Classify this cell by malaria status.
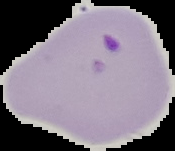

Parasitized.

Summary:
  - Preparation: thin blood film
  - Image size: 175×151 pixels
  - Image type: segmented cell region with the area outside set to black